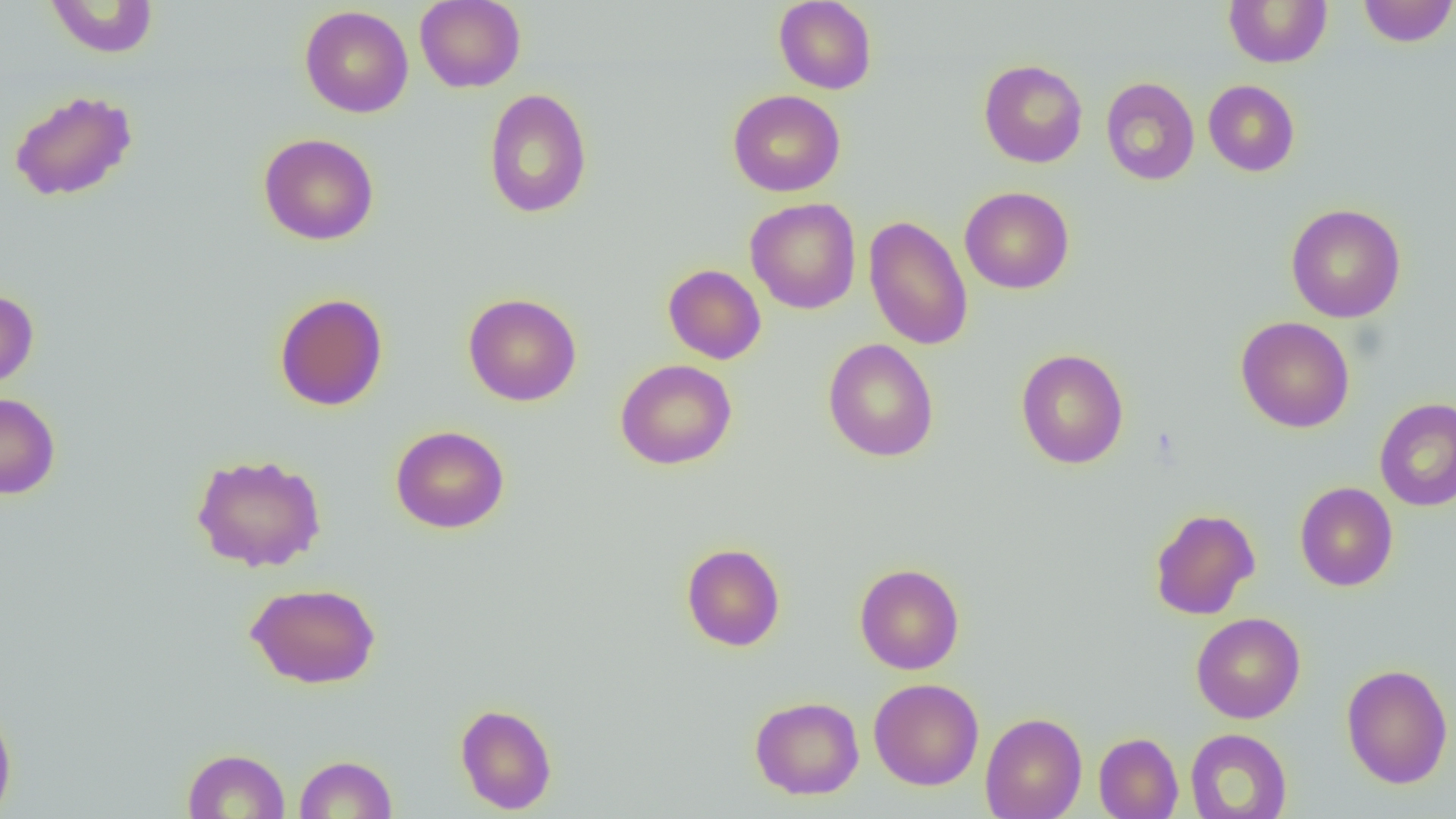 Approximate bounding boxes as (x1,y1)-(x2,y2) corner pairs in pixels. Uninfected red blood cell locations: (45,0)-(159,58), (415,0)-(526,93), (1223,0)-(1333,68), (1357,0)-(1456,47), (774,1)-(877,94), (300,5)-(413,118), (978,59)-(1088,168), (1100,77)-(1200,185), (1203,79)-(1300,176), (483,87)-(593,219), (9,90)-(138,202), (727,90)-(846,197), (258,133)-(379,245), (960,187)-(1074,294), (745,197)-(861,314), (1286,203)-(1406,323), (863,215)-(974,351), (663,264)-(766,364), (0,289)-(39,391), (274,293)-(388,412), (463,293)-(582,407), (1235,316)-(1355,433), (823,338)-(939,462), (1015,348)-(1129,469), (615,359)-(737,470), (0,392)-(60,500), (1374,397)-(1456,511), (390,425)-(510,533), (191,452)-(327,572), (1295,481)-(1398,591), (1149,507)-(1261,620), (681,543)-(785,651), (854,563)-(965,674), (245,582)-(381,689), (1190,612)-(1306,723), (1340,663)-(1453,789), (869,677)-(984,790), (749,696)-(865,799), (0,699)-(17,819), (455,703)-(557,815), (980,712)-(1087,819), (1184,728)-(1293,818), (1093,732)-(1183,819), (182,748)-(291,818), (294,754)-(397,818). Slide-level diagnosis: no evidence of blood parasites. Image is 1456×819 pixels. Thin blood film. 1000x magnification. Light microscopy. One field of a larger specimen.